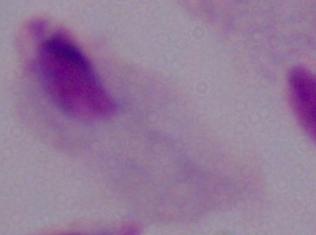
magnification = 1000x
identification = trichomonad
modality = photomicrograph